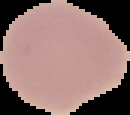

From a thin blood film. Result: negative for malaria parasites. Image is 130×115 pixels. Segmented cell region on a black background.